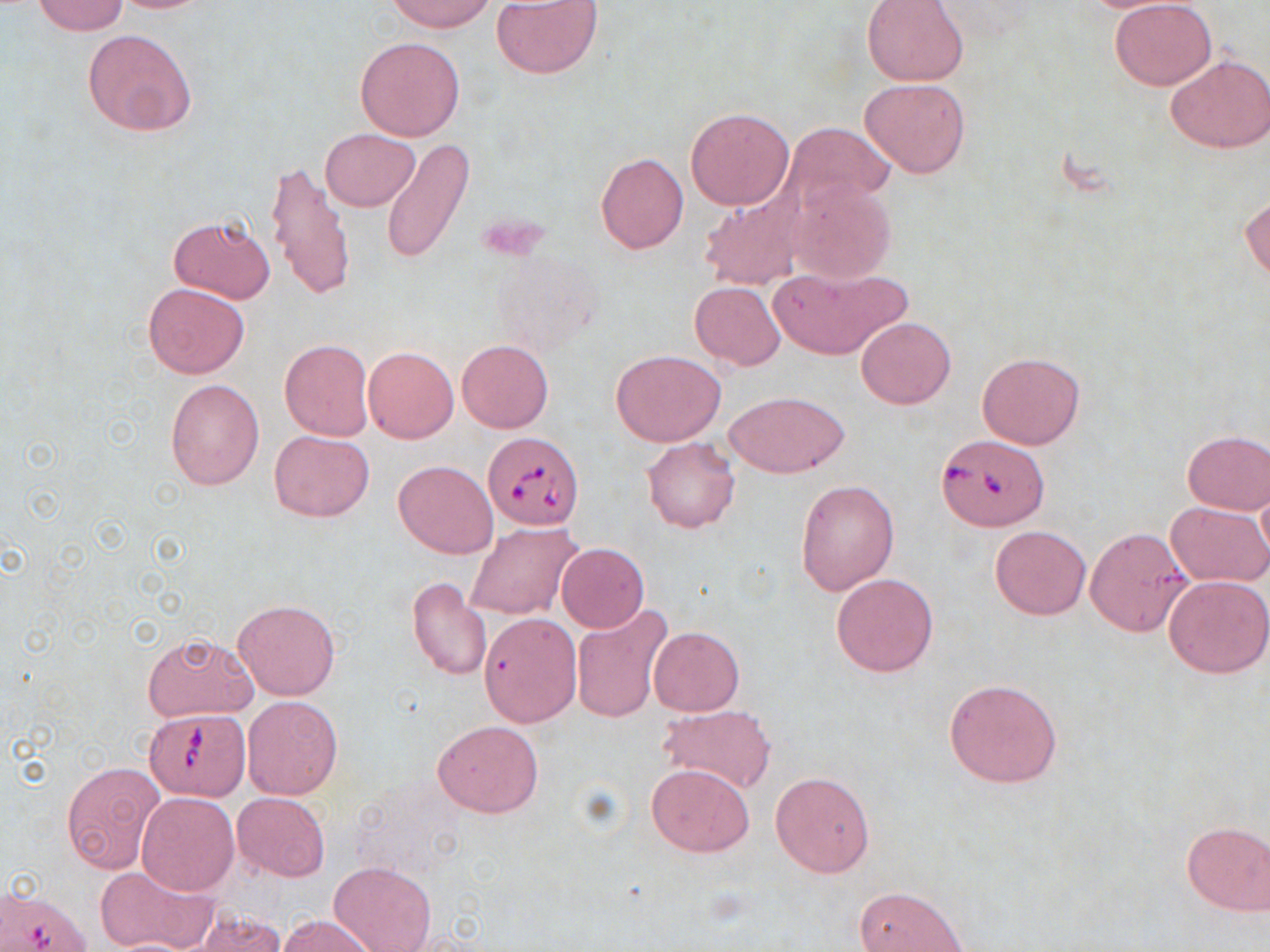

slide-level diagnosis = Babesia divergens
uninfected red blood cell locations = approximate bounding boxes as (x1, y1, x2, y2) in pixels: (32, 0, 129, 34), (388, 0, 495, 33), (491, 1, 603, 78), (861, 1, 968, 85), (1109, 1, 1216, 89), (82, 30, 197, 138), (355, 36, 465, 142), (1165, 53, 1269, 154), (861, 77, 970, 178), (685, 107, 794, 210), (782, 121, 894, 221), (321, 128, 419, 211), (382, 138, 473, 266), (596, 153, 689, 253), (266, 159, 354, 299), (788, 178, 897, 283), (1241, 192, 1269, 282), (699, 194, 803, 290), (168, 215, 275, 305), (769, 264, 907, 360), (690, 281, 787, 369), (143, 283, 250, 377), (857, 317, 955, 409), (279, 339, 374, 440), (457, 339, 553, 433), (363, 346, 458, 443), (610, 349, 725, 446), (977, 352, 1084, 449), (165, 377, 266, 490), (724, 389, 850, 478), (270, 430, 374, 521), (1181, 430, 1270, 514), (642, 437, 739, 532), (393, 459, 498, 558), (797, 478, 900, 595), (1256, 481, 1270, 573), (1166, 500, 1270, 586), (466, 523, 580, 618), (990, 525, 1092, 621), (1086, 527, 1193, 636), (557, 543, 649, 632), (832, 571, 938, 677), (1164, 576, 1269, 678), (408, 578, 493, 682), (234, 599, 339, 700), (572, 605, 671, 723), (479, 612, 581, 726), (648, 626, 744, 716), (142, 632, 257, 723), (945, 678, 1063, 788), (242, 695, 342, 800), (659, 704, 776, 794), (433, 719, 542, 818), (62, 761, 163, 877), (646, 763, 753, 857), (770, 772, 875, 877), (136, 791, 240, 896), (233, 792, 330, 881), (1180, 819, 1270, 915), (329, 860, 436, 952), (94, 865, 216, 952), (854, 886, 967, 952), (188, 910, 290, 952), (276, 914, 377, 952), (103, 937, 201, 951)
Babesia divergens-infected red blood cell locations = approximate bounding boxes as (x1, y1, x2, y2) in pixels: (483, 432, 583, 530), (938, 434, 1047, 531), (146, 710, 250, 799)
image size = 1270×952 pixels
stain = May-Grünwald-Giemsa
modality = optical microscopy
magnification = 1000x
preparation = thin blood smear
field of view = single